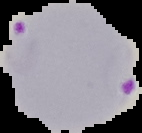

Summary:
  - Image size: 142×133 pixels
  - Image type: segmented cell region with the area outside set to black
  - Preparation: thin blood smear
  - Result: malaria parasites detected